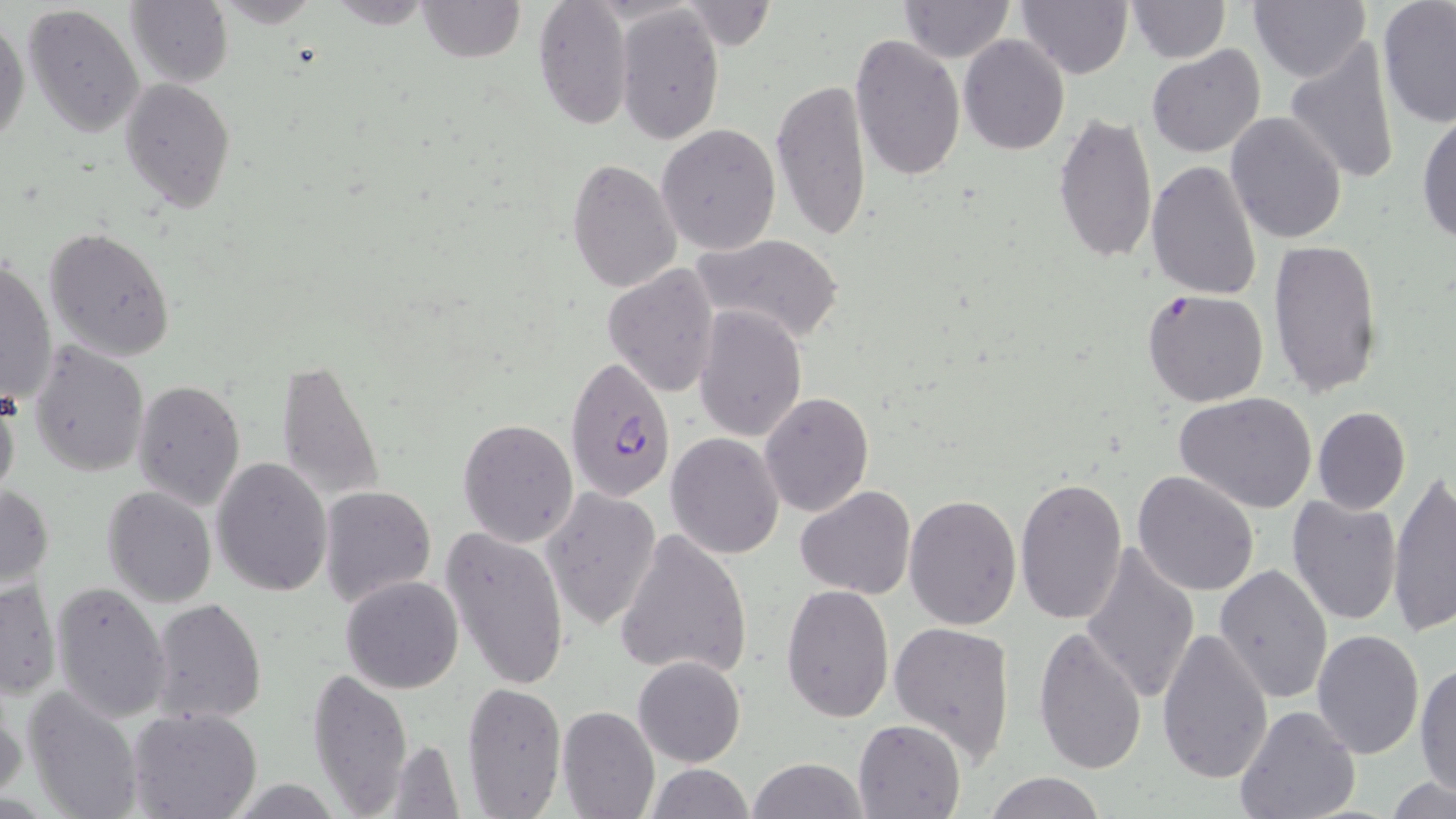
{
  "slide_level_diagnosis": "Plasmodium falciparum",
  "image_size": "1456×819 pixels",
  "plasmodium_falciparum_infected_red_blood_cell_locations": "approximate bounding boxes as named x1/y1/x2/y2 corners in pixels: (x1=564, y1=355, x2=678, y2=501)",
  "modality": "light microscopy",
  "stain": "May-Grünwald-Giemsa",
  "preparation": "thin blood film",
  "magnification": "1000x",
  "uninfected_red_blood_cell_locations": "approximate bounding boxes as named x1/y1/x2/y2 corners in pixels: (x1=126, y1=0, x2=232, y2=88), (x1=325, y1=0, x2=439, y2=29), (x1=416, y1=0, x2=524, y2=63), (x1=532, y1=0, x2=635, y2=131), (x1=898, y1=0, x2=1016, y2=64), (x1=1016, y1=0, x2=1133, y2=79), (x1=1126, y1=0, x2=1230, y2=63), (x1=1248, y1=0, x2=1370, y2=83), (x1=680, y1=1, x2=775, y2=52), (x1=21, y1=2, x2=144, y2=136), (x1=1377, y1=2, x2=1456, y2=128), (x1=616, y1=3, x2=725, y2=145), (x1=0, y1=10, x2=29, y2=148), (x1=847, y1=34, x2=965, y2=182), (x1=959, y1=36, x2=1070, y2=155), (x1=1283, y1=37, x2=1401, y2=186), (x1=1147, y1=45, x2=1265, y2=159), (x1=118, y1=77, x2=236, y2=214), (x1=771, y1=77, x2=874, y2=242), (x1=1416, y1=105, x2=1456, y2=247), (x1=1052, y1=109, x2=1157, y2=264), (x1=1225, y1=112, x2=1347, y2=245), (x1=657, y1=123, x2=781, y2=254), (x1=567, y1=157, x2=682, y2=292), (x1=1145, y1=161, x2=1263, y2=301), (x1=45, y1=226, x2=175, y2=362), (x1=693, y1=232, x2=843, y2=346), (x1=1267, y1=239, x2=1385, y2=397), (x1=1, y1=256, x2=57, y2=406), (x1=603, y1=262, x2=721, y2=398), (x1=1141, y1=289, x2=1270, y2=408), (x1=694, y1=306, x2=807, y2=441), (x1=28, y1=340, x2=149, y2=477), (x1=274, y1=358, x2=385, y2=502), (x1=132, y1=378, x2=247, y2=509), (x1=0, y1=381, x2=21, y2=506), (x1=758, y1=391, x2=874, y2=517), (x1=1175, y1=392, x2=1318, y2=514), (x1=1311, y1=405, x2=1410, y2=514), (x1=457, y1=417, x2=580, y2=547), (x1=666, y1=433, x2=785, y2=558), (x1=210, y1=456, x2=333, y2=596), (x1=1132, y1=471, x2=1259, y2=595), (x1=1387, y1=471, x2=1456, y2=636), (x1=1014, y1=476, x2=1128, y2=624), (x1=0, y1=482, x2=54, y2=596), (x1=319, y1=484, x2=436, y2=607), (x1=102, y1=485, x2=216, y2=607), (x1=542, y1=485, x2=661, y2=631), (x1=796, y1=485, x2=915, y2=599), (x1=904, y1=493, x2=1021, y2=631), (x1=1286, y1=495, x2=1401, y2=626), (x1=439, y1=524, x2=572, y2=692), (x1=614, y1=529, x2=754, y2=681), (x1=1080, y1=540, x2=1198, y2=705), (x1=1213, y1=563, x2=1332, y2=706), (x1=340, y1=576, x2=465, y2=694), (x1=0, y1=578, x2=62, y2=700), (x1=50, y1=580, x2=172, y2=721), (x1=782, y1=583, x2=894, y2=723), (x1=150, y1=598, x2=267, y2=725), (x1=887, y1=622, x2=1018, y2=764), (x1=1033, y1=625, x2=1148, y2=775), (x1=1157, y1=626, x2=1273, y2=782), (x1=1313, y1=628, x2=1425, y2=759), (x1=632, y1=657, x2=745, y2=768), (x1=1414, y1=660, x2=1456, y2=799), (x1=306, y1=666, x2=414, y2=815), (x1=461, y1=680, x2=567, y2=817), (x1=22, y1=685, x2=144, y2=819), (x1=0, y1=698, x2=26, y2=805), (x1=556, y1=704, x2=660, y2=819), (x1=1234, y1=705, x2=1362, y2=819), (x1=128, y1=708, x2=261, y2=819), (x1=853, y1=719, x2=965, y2=818), (x1=381, y1=738, x2=466, y2=816), (x1=747, y1=757, x2=870, y2=818), (x1=644, y1=763, x2=755, y2=818), (x1=983, y1=772, x2=1108, y2=819), (x1=1386, y1=777, x2=1456, y2=818)",
  "field_of_view": "one of a larger specimen"
}